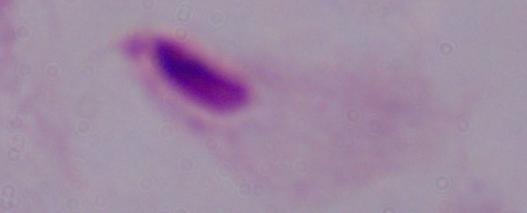

modality: micrograph
magnification: 1000x
identification: trichomonad